Identify the parasite.
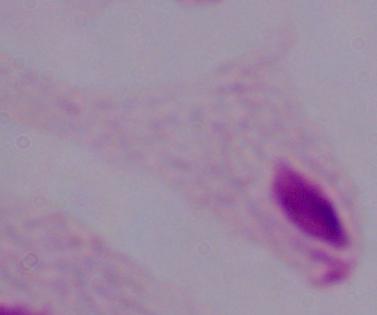

A trichomonad.

Captured at 1000x magnification. Photomicrograph.